Point out each Plasmodium parasite.
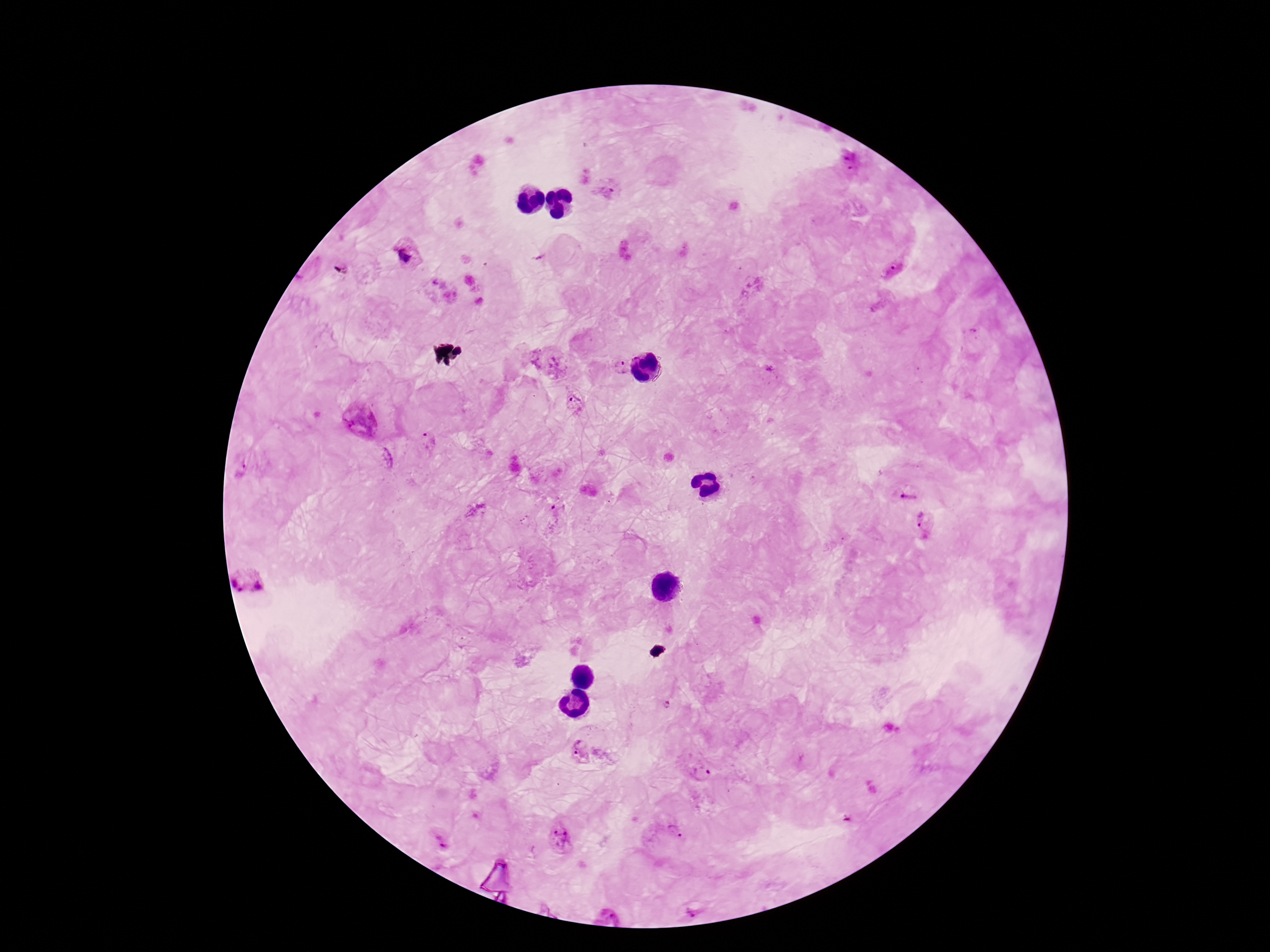
Approximate object centers, in pixels from the top-left corner.
Plasmodium parasites: (x=850, y=161), (x=607, y=192), (x=407, y=254), (x=894, y=269), (x=550, y=360), (x=622, y=366), (x=576, y=399), (x=358, y=419), (x=430, y=441), (x=243, y=467), (x=907, y=492), (x=476, y=512), (x=925, y=521), (x=249, y=579), (x=667, y=705), (x=581, y=751), (x=698, y=770), (x=675, y=830), (x=559, y=836), (x=439, y=841).

Summary:
  - Stain: Giemsa
  - Magnification: 100x
  - Capture: smartphone camera through the microscope eyepiece
  - Patient malaria status: infected
  - Preparation: thick peripheral-blood smear
  - Image size: 1270×952 pixels
  - Field of view: single